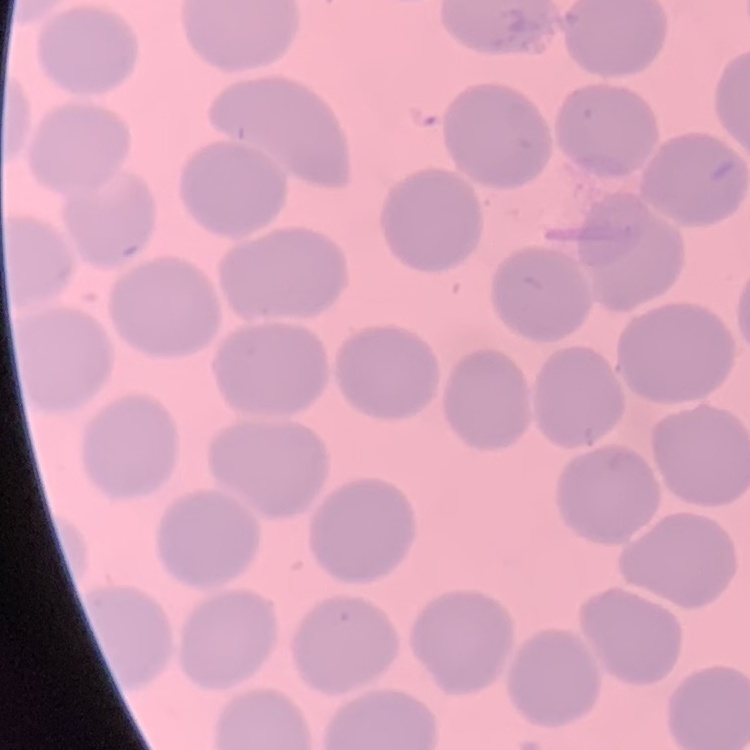

{
  "red_blood_cell_morphology": "no rouleaux formation",
  "image_type": "square crop of a larger photomicrograph",
  "preparation": "thin blood film",
  "stain": "Field's or Giemsa"
}